Name the parasite shown.
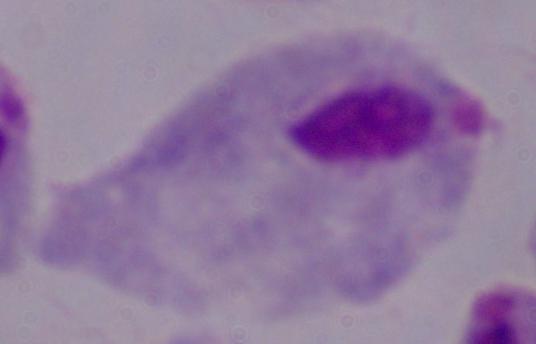

This is a trichomonad.

magnification: 1000x
modality: photomicrograph